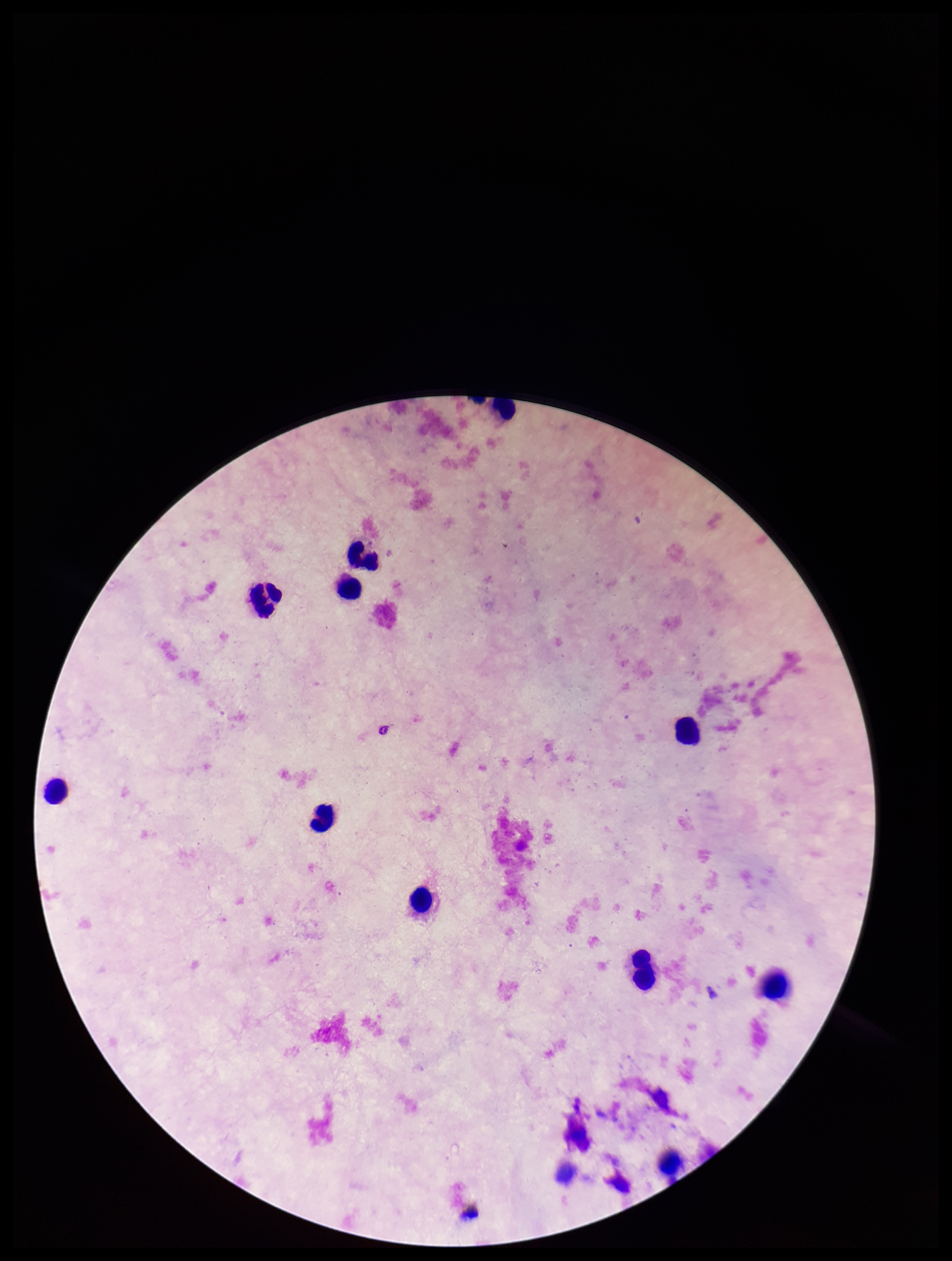

preparation: thick
image_size: 952×1261 pixels
patient_malaria_status: negative
capture: smartphone photograph through the microscope eyepiece
stain: Giemsa
leukocyte_count: 11
field_of_view: one from this slide
plasmodium_parasites: none seen
parasite_count: 0